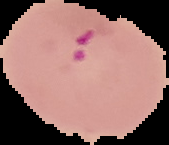
Summary:
  - Image type: segmented cell region with the area outside set to black
  - Image size: 169×145 pixels
  - Preparation: thin blood film
  - Malaria status: parasitized